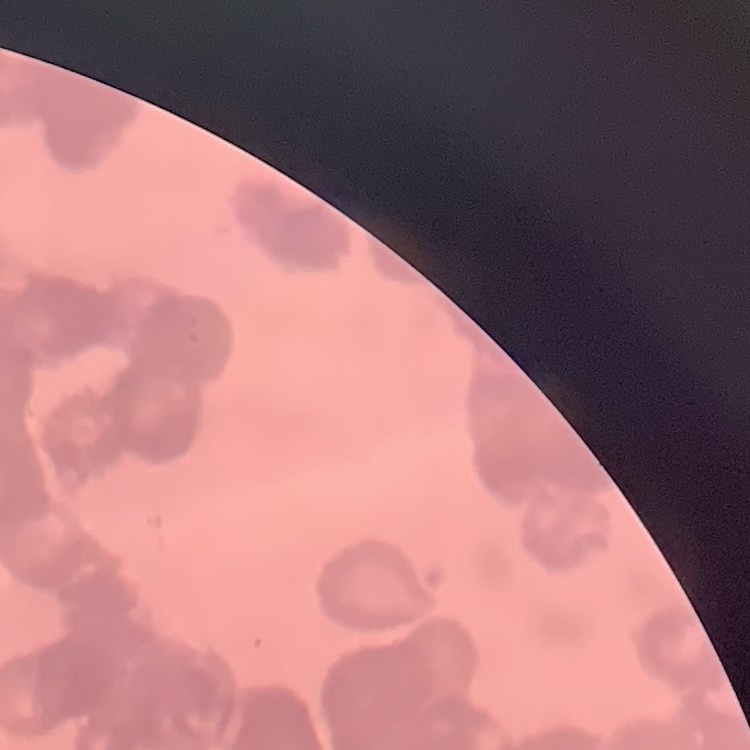

red_blood_cell_morphology: rouleaux formation
stain: Field's or Giemsa
image_type: square crop of a larger photomicrograph
preparation: thin blood smear